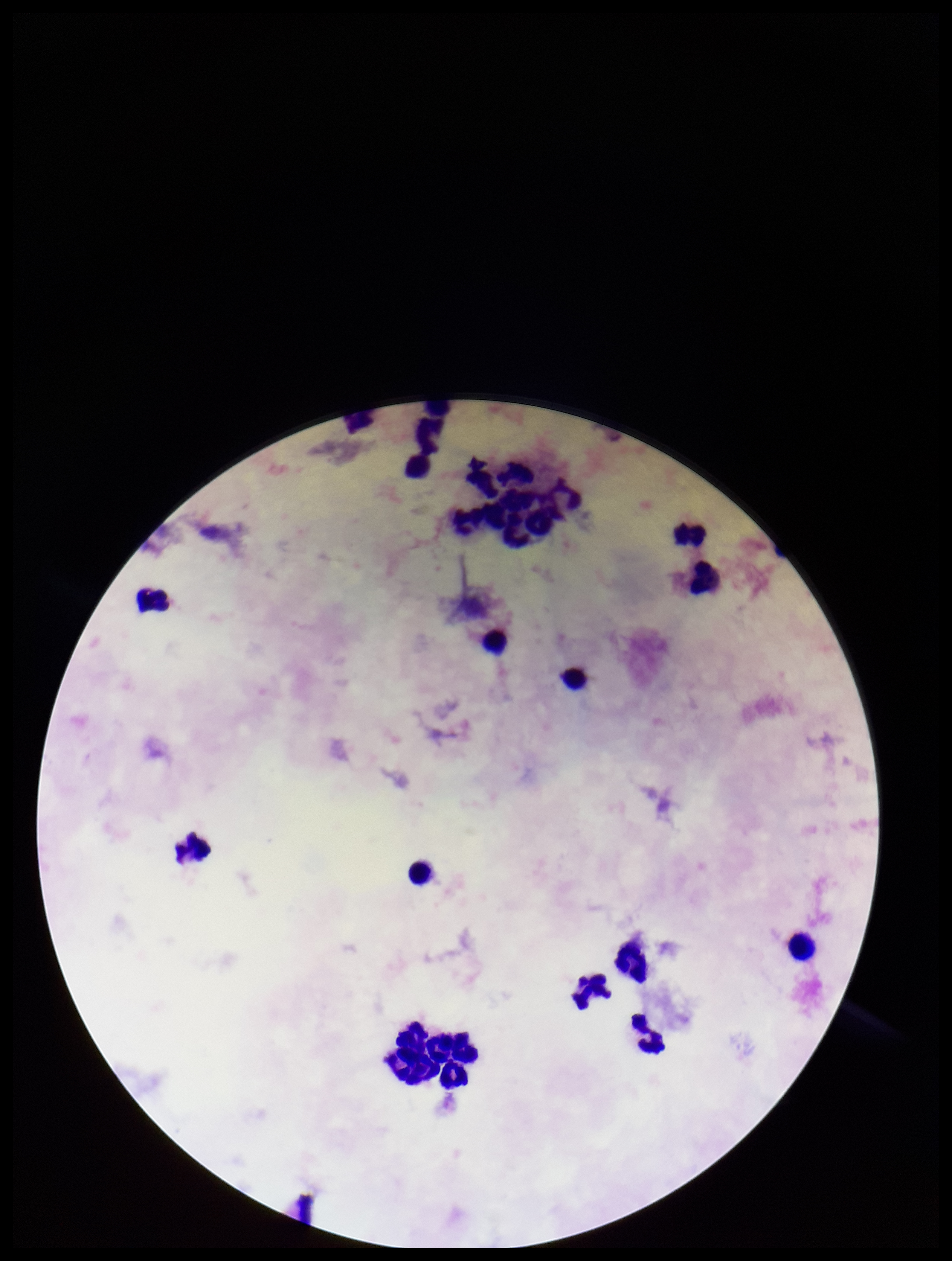
Summary:
  - Image size: 952×1261 pixels
  - Preparation: thick
  - Capture: smartphone photograph through the microscope eyepiece
  - Stain: Giemsa
  - Parasite count: 0
  - Patient malaria status: negative
  - Leukocyte count: 21
  - Plasmodium parasites: none identified
  - Field of view: single